Identify the parasite.
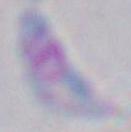

This is Toxoplasma gondii.

Summary:
  - Modality: micrograph
  - Magnification: 1000x